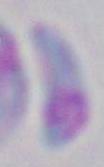

magnification: 1000x
identification: Toxoplasma gondii
modality: photomicrograph